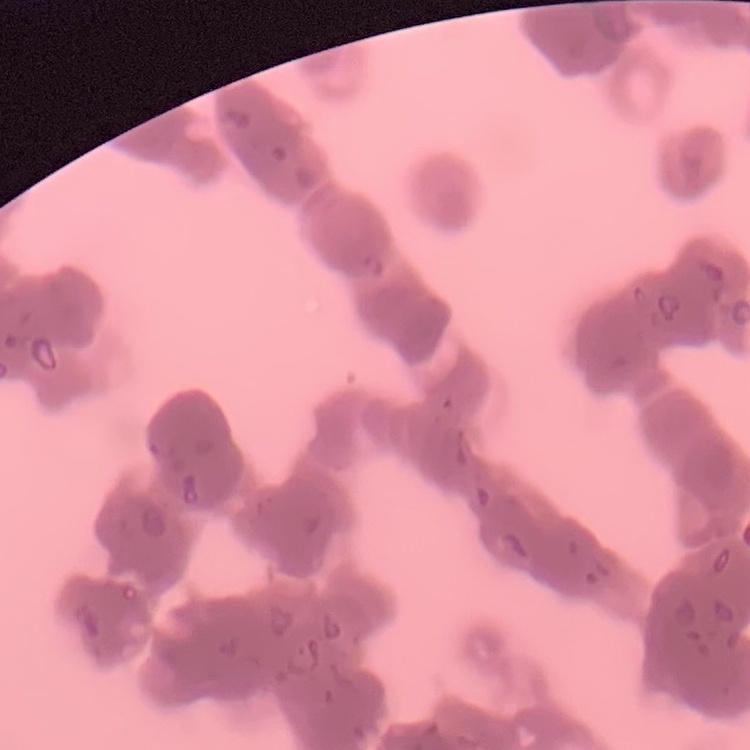

Summary:
  - Erythrocyte morphology: rouleaux formation
  - Image type: square crop of a larger photomicrograph
  - Stain: Field's or Giemsa
  - Preparation: thin blood smear